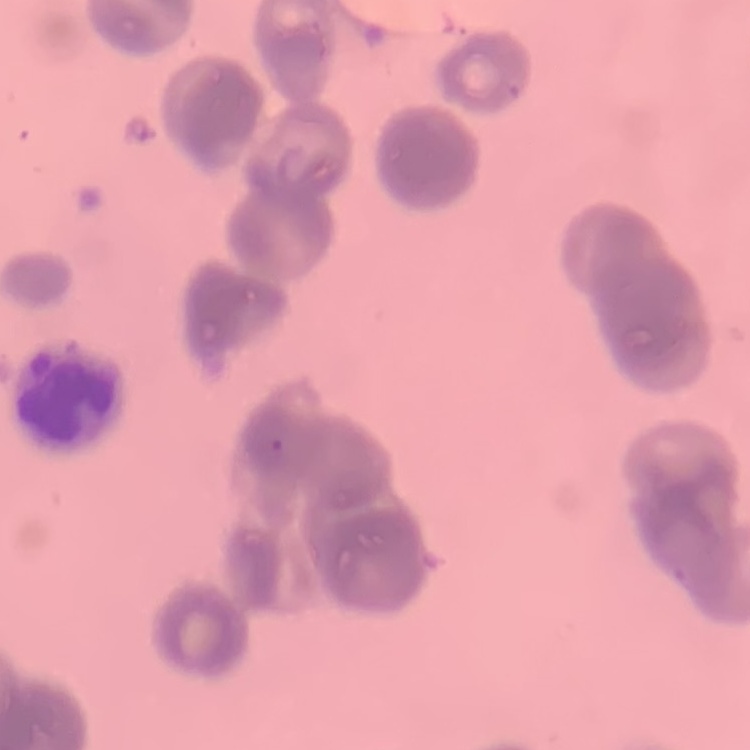

The red blood cells show rouleaux formation. Thin blood film. One tile cut from a larger photomicrograph. Field's or Giemsa stain.